Name the blood parasite species.
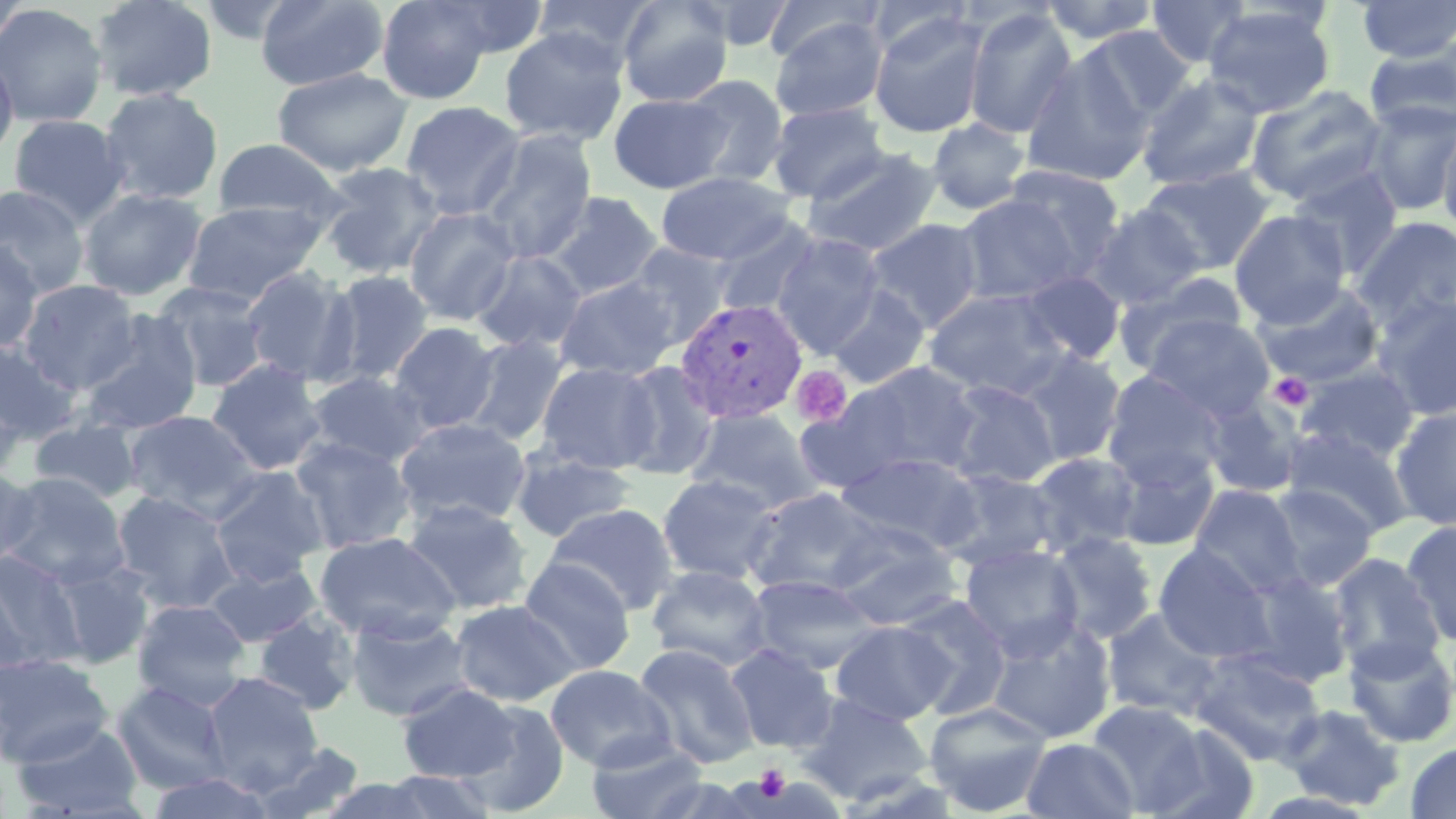

Plasmodium vivax.

{
  "stain": "May-Grünwald-Giemsa",
  "uninfected_red_blood_cell_locations": "approximate bounding boxes as (x1,y1)-(x2,y2) corner pairs in pixels: (0,0)-(29,53), (90,0)-(218,102), (255,0)-(389,91), (376,0)-(494,104), (429,0)-(550,59), (532,0)-(658,68), (617,0)-(733,107), (692,0)-(798,52), (1039,0)-(1163,45), (1146,0)-(1252,68), (765,1)-(880,66), (865,1)-(972,61), (1355,1)-(1456,62), (0,4)-(108,128), (1203,5)-(1336,118), (963,7)-(1078,140), (869,11)-(990,139), (770,15)-(888,121), (1080,25)-(1196,125), (498,27)-(630,147), (1363,41)-(1456,135), (1021,49)-(1156,188), (0,52)-(18,164), (272,68)-(413,177), (1137,73)-(1265,192), (681,75)-(790,187), (1246,84)-(1389,206), (99,88)-(224,205), (608,92)-(731,193), (400,100)-(525,219), (1361,100)-(1456,216), (767,101)-(889,204), (8,114)-(129,227), (927,118)-(1031,215), (1437,125)-(1456,236), (475,128)-(598,263), (211,138)-(346,226), (802,146)-(943,258), (316,162)-(446,280), (997,164)-(1126,281), (1138,166)-(1275,275), (1287,166)-(1404,277), (655,171)-(796,265), (0,185)-(90,298), (79,188)-(206,301), (543,192)-(663,299), (955,192)-(1090,306), (181,199)-(329,305), (1088,204)-(1207,310), (403,206)-(521,326), (1230,209)-(1351,327), (1352,216)-(1456,331), (710,217)-(822,320), (865,218)-(986,333), (771,233)-(885,358), (0,240)-(43,354), (626,241)-(733,346), (472,250)-(588,354), (242,265)-(358,385), (323,270)-(435,386), (1019,271)-(1126,365), (1114,271)-(1249,376), (555,276)-(681,381), (19,279)-(140,393), (1253,281)-(1385,390), (152,282)-(271,392), (826,285)-(931,390), (923,287)-(1071,400), (1371,295)-(1456,420), (80,310)-(204,434), (1144,314)-(1276,420), (389,322)-(501,433), (462,335)-(568,446), (0,339)-(82,443), (1016,348)-(1127,465), (207,358)-(328,475), (536,361)-(661,473), (614,361)-(719,480), (809,362)-(987,486), (1295,363)-(1420,465), (1101,370)-(1224,488), (304,371)-(432,469), (943,380)-(1060,489), (0,381)-(31,480), (1199,395)-(1305,499), (1390,406)-(1456,531), (686,407)-(822,512), (122,410)-(261,516), (28,417)-(145,503), (395,418)-(531,525), (1282,428)-(1416,539), (289,436)-(416,554), (1111,446)-(1218,551), (509,447)-(636,543), (1026,451)-(1144,557), (838,452)-(979,549), (0,465)-(39,569), (208,466)-(329,587), (936,467)-(1061,570), (2,473)-(130,589), (656,474)-(780,584), (1264,484)-(1377,592), (1190,485)-(1305,596), (744,486)-(879,598), (111,490)-(240,613), (402,498)-(534,614), (546,503)-(679,616), (831,521)-(960,629), (1401,521)-(1456,649), (314,531)-(461,642), (1047,531)-(1159,645), (960,543)-(1083,660), (1154,544)-(1276,664), (0,551)-(83,672), (1327,552)-(1445,677), (45,557)-(156,670), (517,557)-(636,676), (204,560)-(323,648), (646,564)-(772,671), (1241,570)-(1354,687), (746,574)-(880,675), (897,594)-(1012,719), (131,599)-(251,709), (449,599)-(580,706), (1102,608)-(1222,720), (252,611)-(360,715), (344,611)-(476,723), (986,616)-(1116,745), (831,620)-(954,725), (1343,636)-(1456,748), (633,643)-(759,769), (725,643)-(839,753), (1189,647)-(1326,766), (0,653)-(113,768), (545,663)-(674,772), (204,673)-(323,790), (111,681)-(232,794), (396,682)-(520,782), (797,693)-(933,804), (458,699)-(570,817), (1086,699)-(1209,814), (924,701)-(1053,816), (1278,703)-(1406,810), (10,721)-(146,818), (1142,722)-(1258,817), (585,737)-(711,819), (1022,737)-(1139,819), (250,741)-(366,819), (1405,741)-(1456,819), (378,769)-(499,819), (144,772)-(277,818), (639,773)-(769,818), (317,777)-(441,819)",
  "magnification": "1000x",
  "modality": "light microscopy",
  "image_size": "1456×819 pixels",
  "plasmodium_vivax_infected_red_blood_cell_locations": "approximate bounding boxes as (x1,y1)-(x2,y2) corner pairs in pixels: (673,298)-(807,424)",
  "preparation": "thin blood smear",
  "field_of_view": "single",
  "platelet_locations": "approximate bounding boxes as (x1,y1)-(x2,y2) corner pairs in pixels: (791,365)-(853,428), (1269,372)-(1313,411), (754,764)-(791,802)"
}